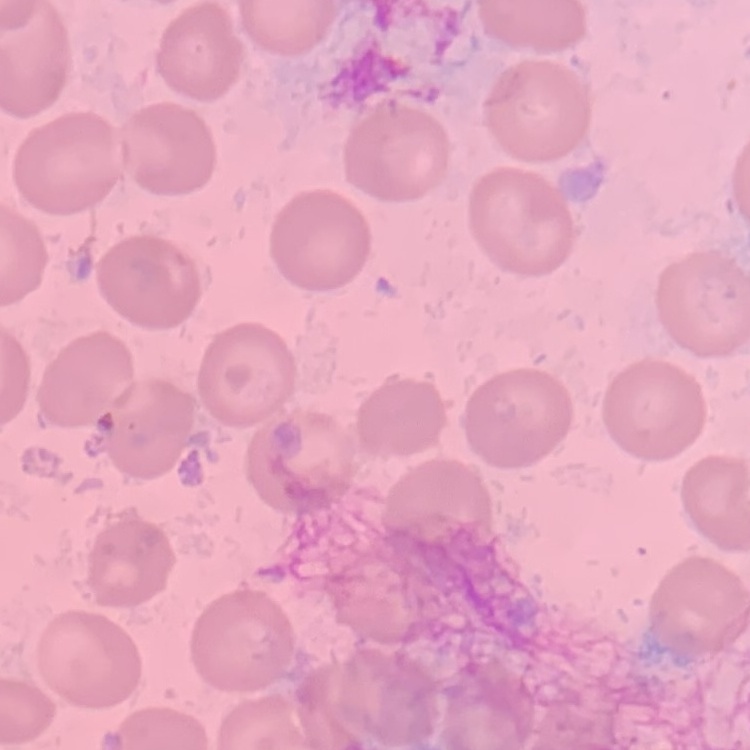

Summary:
  - Erythrocyte morphology: no rouleaux formation
  - Preparation: thin blood film
  - Image type: square crop of a larger photomicrograph
  - Stain: Field's or Giemsa